State which parasite is depicted.
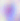

This is Toxoplasma gondii.

Photomicrograph. Captured at 400x magnification.